Point out each Plasmodium parasite and each leukocyte.
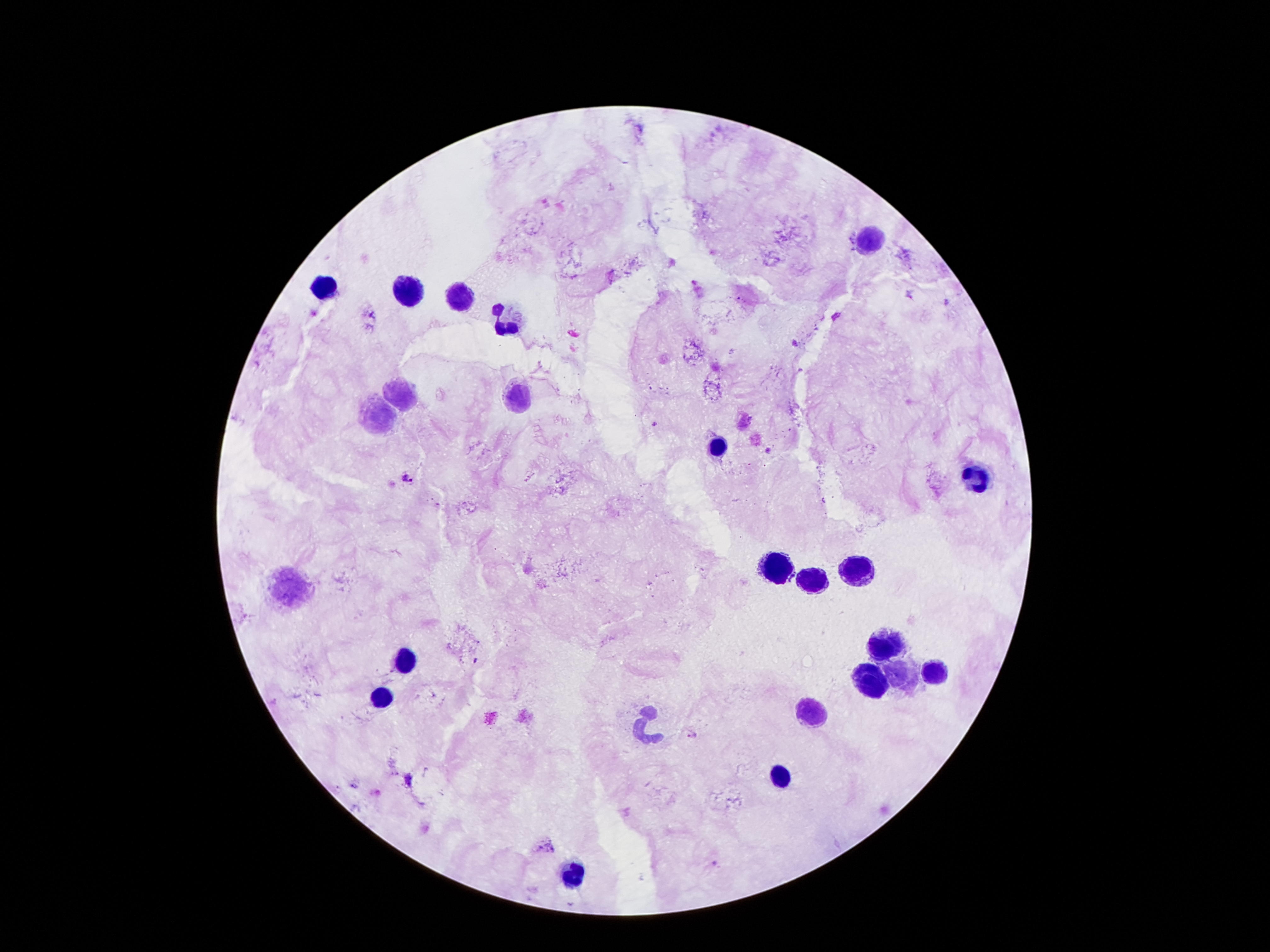
Approximate centers as [x, y] in pixels.
Plasmodium parasites: [654, 424], [768, 450], [407, 479], [691, 732], [547, 847].
Leukocytes: [873, 239], [325, 288], [407, 290], [460, 299], [511, 321], [400, 392], [519, 403], [380, 416], [718, 447], [977, 478], [858, 566], [780, 569], [814, 580], [294, 591], [886, 644], [407, 661], [935, 672], [898, 675], [869, 683], [385, 694], [807, 712], [646, 725], [780, 776], [577, 873].

Giemsa-stained preparation. Thick blood smear. Image is 1270×952 pixels. Smartphone photograph taken through the microscope eyepiece. Single field of view. 100x magnification. Patient malaria status: infected with Plasmodium falciparum.